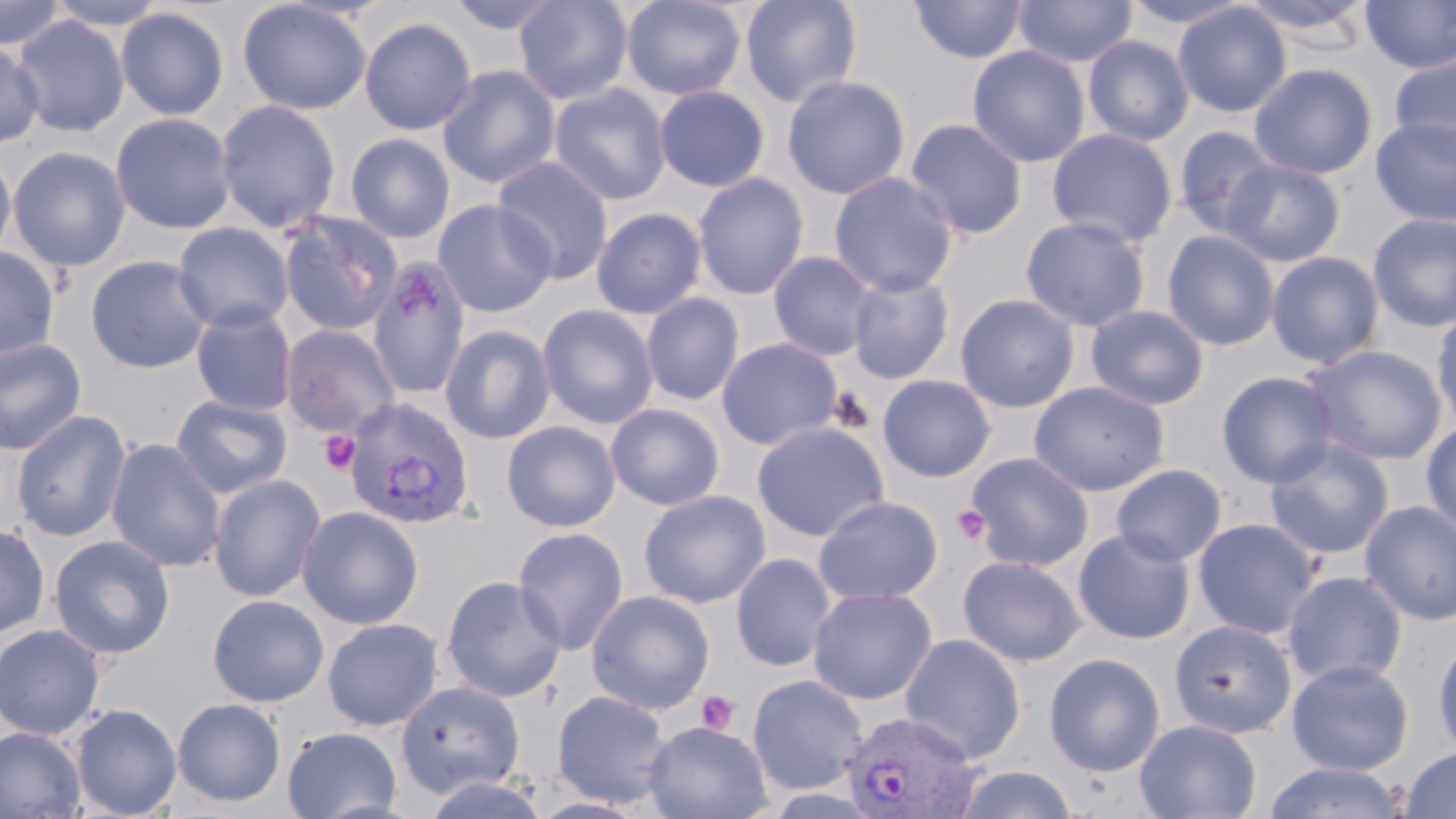
Summary:
  - Coordinate format: approximate bounding boxes as (x1, y1, x2, y2) in pixels
  - Platelet locations: (319, 430, 361, 476), (952, 504, 993, 547), (697, 690, 740, 734)
  - Uninfected red blood cell locations: (0, 0, 67, 51), (45, 0, 171, 30), (238, 0, 372, 115), (444, 0, 568, 35), (513, 0, 634, 105), (621, 0, 747, 100), (739, 0, 863, 108), (1013, 0, 1137, 68), (1120, 0, 1252, 29), (1239, 0, 1376, 39), (909, 1, 1027, 64), (1359, 1, 1456, 74), (1173, 3, 1291, 118), (116, 7, 229, 120), (11, 15, 129, 137), (358, 17, 477, 136), (1082, 35, 1194, 146), (0, 40, 44, 149), (967, 45, 1090, 168), (1388, 54, 1456, 163), (437, 64, 560, 189), (1249, 64, 1377, 179), (781, 75, 910, 200), (549, 83, 671, 206), (653, 85, 770, 192), (215, 99, 341, 233), (110, 113, 236, 234), (1370, 116, 1456, 228), (904, 118, 1028, 240), (1172, 126, 1281, 237), (1046, 128, 1177, 248), (345, 132, 455, 243), (0, 146, 16, 268), (7, 146, 130, 272), (492, 156, 614, 285), (1221, 158, 1345, 266), (828, 172, 958, 297), (692, 173, 810, 301), (432, 199, 557, 318), (591, 207, 707, 319), (279, 213, 403, 336), (1367, 214, 1456, 332), (1020, 216, 1150, 332), (173, 223, 294, 334), (1162, 230, 1280, 351), (0, 247, 59, 363), (768, 251, 878, 362), (1266, 251, 1384, 368), (85, 255, 213, 373), (368, 260, 472, 399), (847, 272, 955, 384), (641, 293, 745, 406), (955, 294, 1080, 412), (537, 303, 659, 430), (1085, 305, 1209, 410), (1431, 305, 1456, 433), (190, 307, 297, 416), (281, 325, 400, 438), (440, 325, 555, 444), (0, 338, 87, 455), (716, 338, 843, 450), (1303, 345, 1447, 466), (1216, 371, 1340, 488), (877, 374, 996, 482), (1028, 381, 1169, 496), (171, 395, 292, 499), (605, 403, 726, 510), (11, 410, 132, 543), (1420, 420, 1456, 536), (502, 421, 621, 532), (751, 421, 890, 541), (106, 438, 226, 572), (1264, 438, 1394, 560), (966, 452, 1094, 571), (1111, 464, 1227, 566), (208, 474, 326, 602), (638, 489, 771, 608), (813, 496, 943, 605), (1359, 500, 1456, 625), (297, 506, 424, 629), (1192, 518, 1320, 639), (0, 523, 50, 638), (512, 526, 629, 655), (1073, 529, 1196, 644), (48, 534, 175, 660), (731, 552, 837, 672), (958, 555, 1087, 667), (1282, 571, 1408, 688), (441, 575, 567, 702), (807, 587, 938, 705), (586, 590, 716, 714), (207, 595, 329, 707), (323, 618, 443, 731), (1168, 619, 1297, 738), (0, 624, 106, 739), (900, 633, 1025, 763), (1432, 636, 1456, 761), (1044, 653, 1165, 776), (1286, 660, 1413, 776), (747, 675, 868, 795), (395, 681, 526, 799), (551, 690, 673, 809), (172, 698, 286, 806), (71, 704, 181, 818), (1134, 719, 1262, 819), (643, 720, 773, 819), (0, 727, 86, 819), (282, 727, 402, 819), (1400, 746, 1456, 819), (1261, 761, 1410, 818), (953, 765, 1078, 819), (421, 774, 549, 817)
  - Plasmodium vivax-infected red blood cell locations: (344, 397, 474, 530), (840, 711, 981, 817)
  - Slide-level diagnosis: Plasmodium vivax
  - Stain: May-Grünwald-Giemsa
  - Preparation: thin blood film
  - Modality: light microscopy
  - Field of view: one of a larger specimen
  - Magnification: 1000x
  - Image size: 1456×819 pixels